Report the malaria status of this cell.
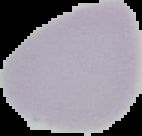

It is uninfected.

{
  "preparation": "thin blood smear",
  "image_size": "142×136 pixels",
  "image_type": "cell region segmented out of the field of view; surrounding area masked to black"
}